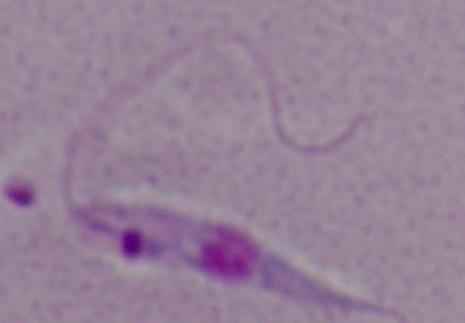
magnification = 1000x
modality = micrograph
identification = Leishmania